Describe the morphology of the red blood cells.
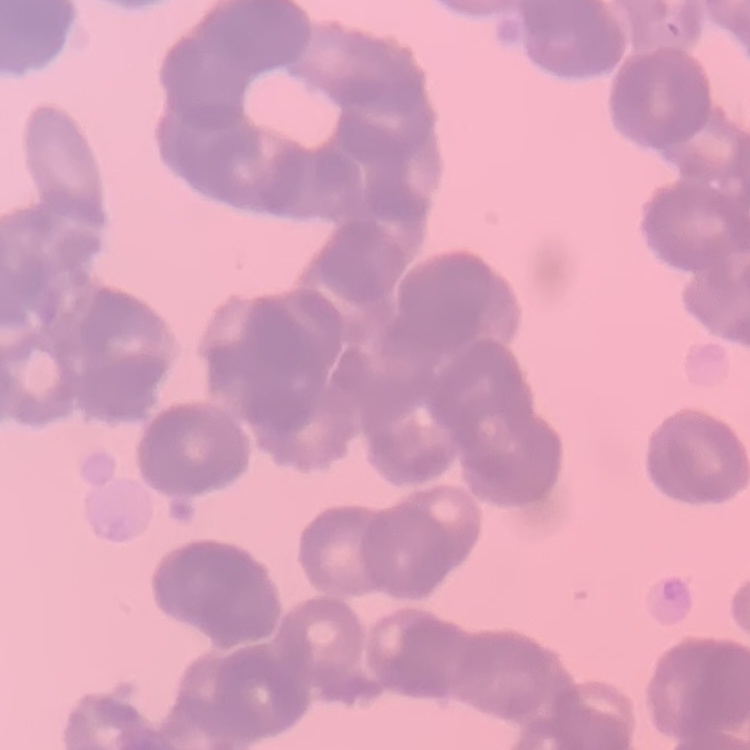
Rouleaux formation.

image type = square crop of a larger photomicrograph
stain = Field's or Giemsa
preparation = thin blood smear